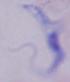

Summary:
  - Modality: micrograph
  - Identification: trypanosome
  - Magnification: 1000x